Locate every malaria parasite and every leukocyte.
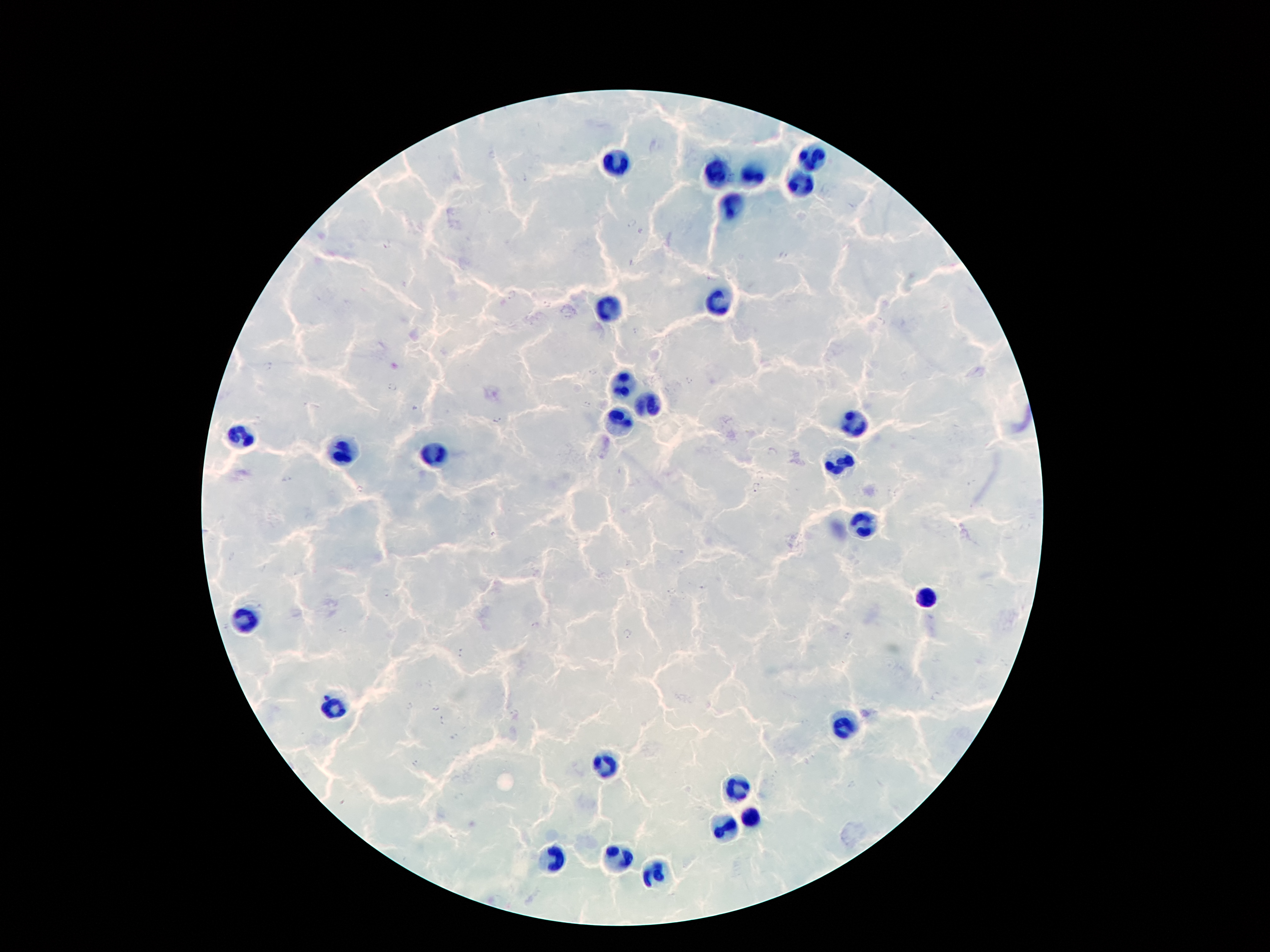
Approximate object centers, in pixels from the top-left corner.
Malaria parasites: (x=525, y=178), (x=631, y=224), (x=388, y=245), (x=782, y=256), (x=512, y=296), (x=547, y=305), (x=636, y=330), (x=268, y=368), (x=593, y=372), (x=689, y=380), (x=391, y=387), (x=587, y=406), (x=413, y=408), (x=497, y=419), (x=772, y=451), (x=760, y=476), (x=287, y=478), (x=755, y=486), (x=360, y=490), (x=492, y=535), (x=671, y=591), (x=388, y=593), (x=536, y=624), (x=627, y=633), (x=849, y=635), (x=462, y=652), (x=937, y=696), (x=408, y=706), (x=437, y=708), (x=442, y=721), (x=455, y=737), (x=414, y=762), (x=852, y=785).
Leukocytes: (x=811, y=159), (x=617, y=166), (x=752, y=174), (x=718, y=176), (x=802, y=185), (x=732, y=204), (x=721, y=301), (x=609, y=309), (x=624, y=381), (x=645, y=404), (x=620, y=421), (x=854, y=421), (x=242, y=439), (x=342, y=454), (x=434, y=454), (x=841, y=464), (x=861, y=521), (x=925, y=597), (x=242, y=615), (x=335, y=706), (x=844, y=729), (x=602, y=765), (x=737, y=790), (x=754, y=814), (x=731, y=831), (x=551, y=855), (x=617, y=855), (x=655, y=872).

Summary:
  - Preparation: thick blood film
  - Field of view: single
  - Image size: 1270×952 pixels
  - Patient malaria status: infected with Plasmodium falciparum
  - Stain: Giemsa
  - Magnification: 100x
  - Capture: smartphone through the microscope eyepiece